Comment on the morphology of the erythrocytes.
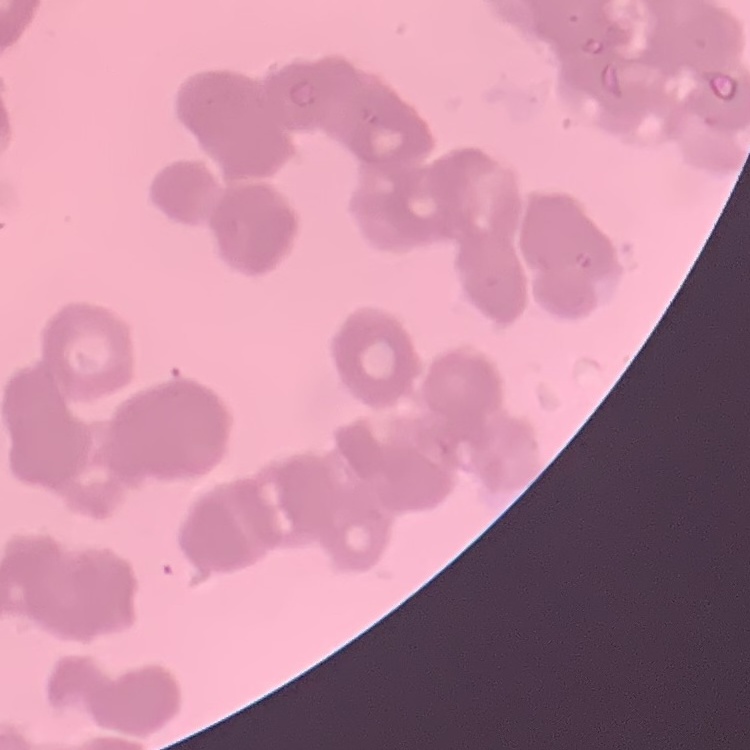

Rouleaux formation.

image type = square crop of a larger photomicrograph
stain = Field's or Giemsa
preparation = thin blood film